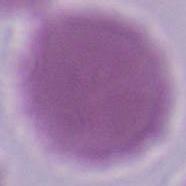
Summary:
  - Identification: red blood cell
  - Modality: photomicrograph
  - Magnification: 1000x